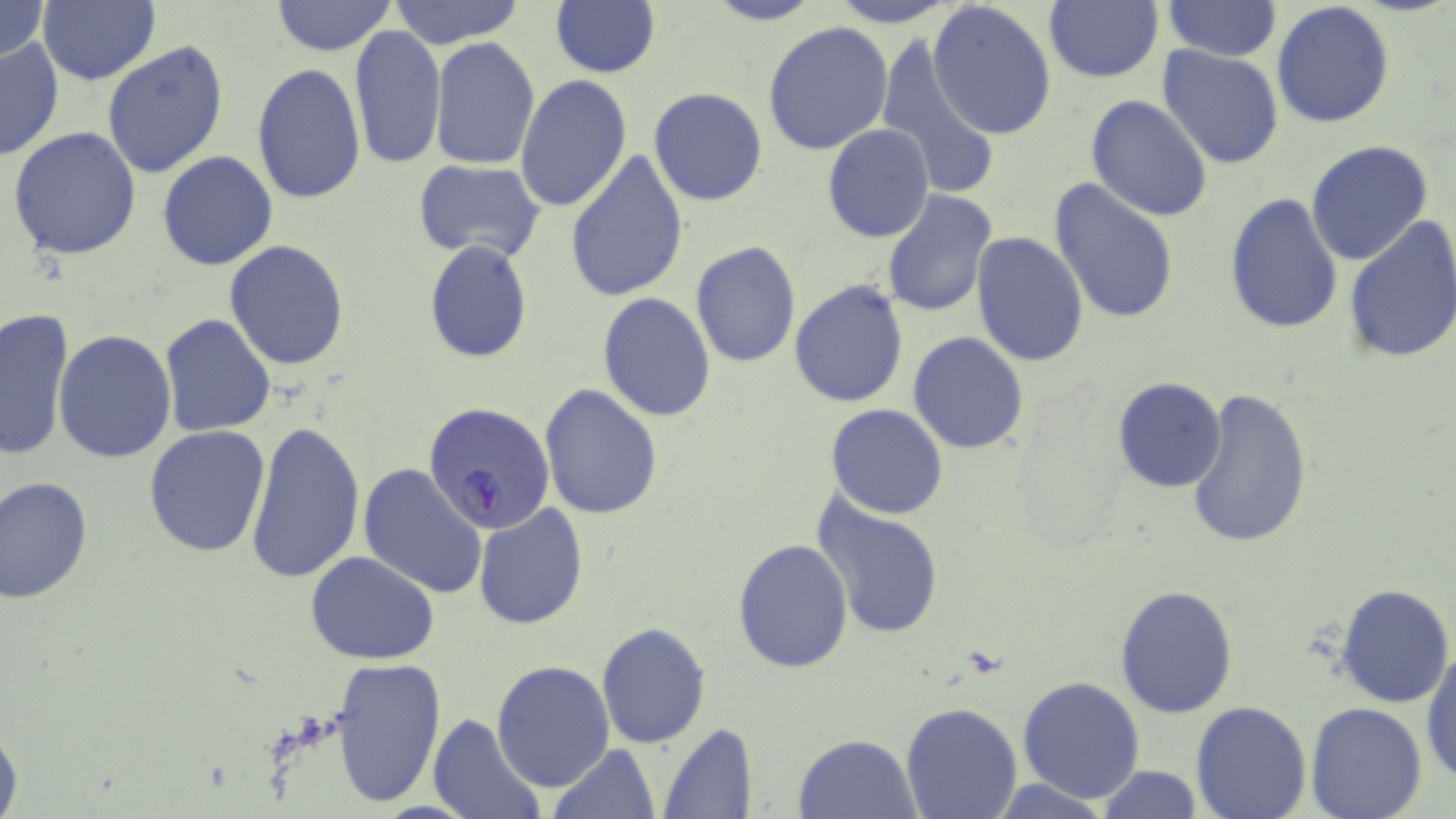
slide_level_diagnosis: Plasmodium falciparum
stain: May-Grünwald-Giemsa
magnification: 1000x
image_size: 1456×819 pixels
preparation: thin blood film
uninfected_red_blood_cell_locations: 'approximate bounding boxes as [x1, y1, x2, y2] in pixels: [40, 0, 159, 85], [270, 0, 397, 56], [386, 0, 528, 49], [702, 0, 826, 25], [827, 0, 959, 26], [1044, 0, 1163, 83], [1163, 0, 1282, 59], [0, 1, 51, 63], [928, 1, 1058, 141], [550, 2, 662, 78], [1272, 2, 1395, 130], [762, 21, 897, 157], [349, 26, 446, 171], [873, 34, 1000, 205], [0, 35, 65, 163], [429, 38, 541, 172], [103, 40, 230, 179], [1158, 45, 1285, 169], [251, 64, 366, 205], [514, 74, 632, 214], [648, 88, 769, 207], [1086, 94, 1214, 222], [822, 123, 934, 242], [7, 126, 143, 262], [1306, 140, 1435, 266], [565, 149, 690, 301], [157, 151, 278, 271], [411, 160, 549, 266], [1049, 178, 1180, 324], [880, 192, 996, 318], [1225, 192, 1345, 333], [1341, 216, 1456, 364], [971, 231, 1090, 366], [224, 240, 350, 371], [424, 240, 532, 363], [691, 241, 801, 368], [789, 279, 909, 407], [597, 293, 716, 421], [1, 306, 77, 459], [157, 313, 277, 438], [54, 331, 177, 463], [908, 332, 1029, 455], [1113, 377, 1228, 493], [539, 383, 665, 520], [1185, 387, 1314, 551], [825, 404, 949, 519], [246, 419, 366, 584], [143, 425, 270, 559], [358, 463, 488, 599], [1, 476, 96, 605], [813, 491, 947, 642], [473, 503, 590, 629], [733, 538, 854, 672], [305, 551, 440, 663], [1335, 582, 1454, 707], [1115, 586, 1239, 718], [595, 622, 711, 748], [518, 632, 684, 766], [1422, 643, 1455, 787], [330, 656, 446, 810], [492, 660, 615, 791], [1017, 676, 1145, 804], [1190, 701, 1313, 819], [901, 703, 1021, 819], [1305, 703, 1429, 819], [429, 714, 543, 819], [0, 718, 24, 818], [659, 724, 758, 818], [794, 733, 920, 817], [549, 742, 660, 819], [1093, 765, 1203, 819]'
field_of_view: single
plasmodium_falciparum_infected_red_blood_cell_locations: 'approximate bounding boxes as [x1, y1, x2, y2] in pixels: [426, 404, 555, 534]'
modality: optical microscopy